Name the parasite shown.
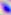
Toxoplasma gondii.

modality = micrograph
magnification = 400x